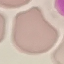 Malaria status: uninfected. Acquired by smartphone through the microscope eyepiece. Giemsa-stained preparation. Thin smear of blood. Automatically extracted cell patch, resized to 64 × 64 pixels.